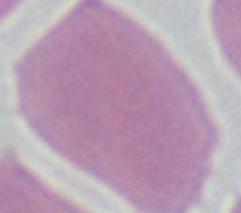 A red blood cell is shown. Photomicrograph. 1000x magnification.